Name the blood parasite species.
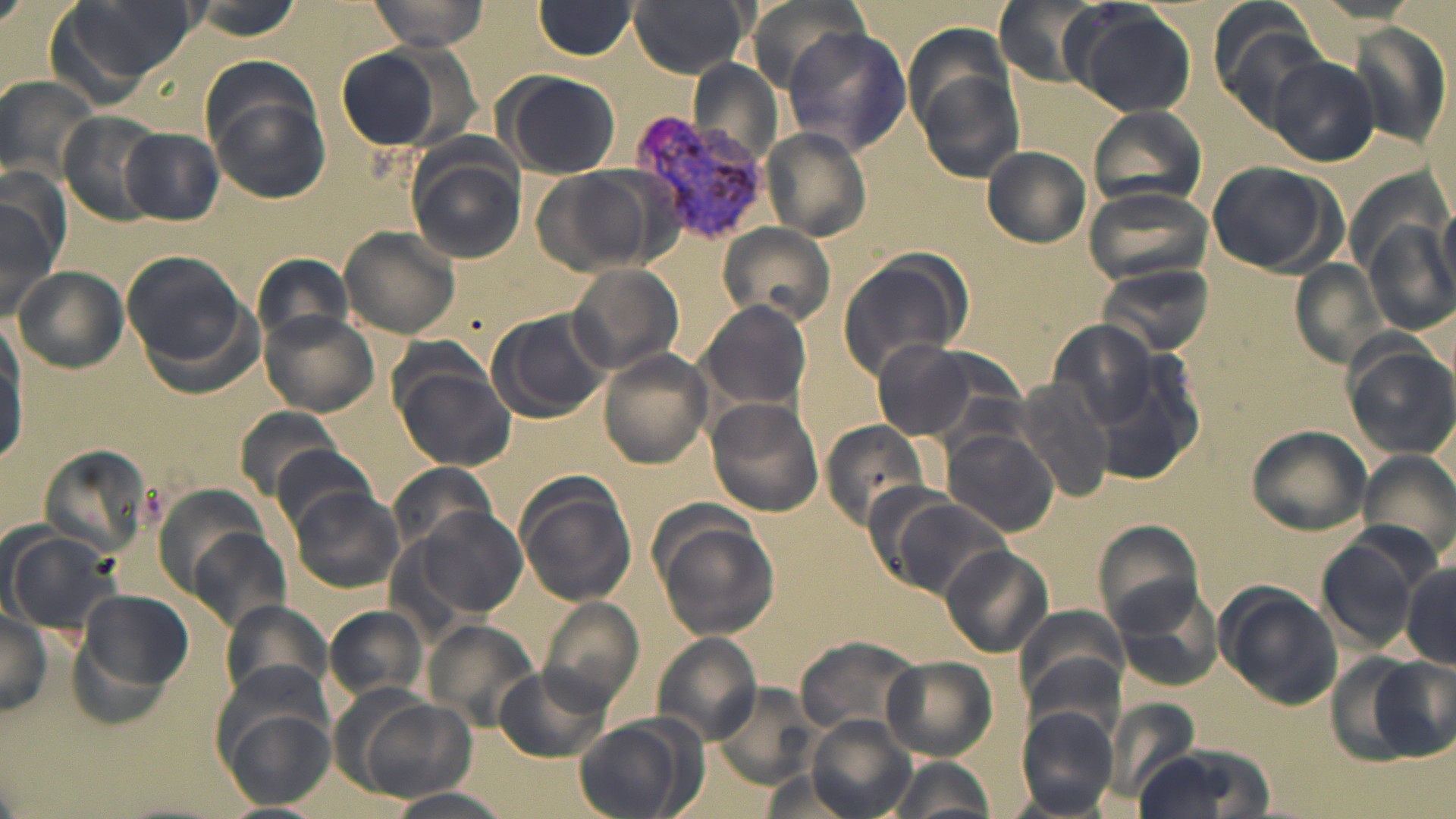
Plasmodium vivax.

preparation: thin blood smear
modality: light microscopy
image_size: 1456×819 pixels
uninfected_red_blood_cell_locations: 'approximate bounding boxes as named x1/y1/x2/y2 corners in pixels: (x1=49, y1=0, x2=195, y2=100), (x1=365, y1=0, x2=487, y2=51), (x1=628, y1=0, x2=749, y2=77), (x1=992, y1=0, x2=1108, y2=86), (x1=535, y1=1, x2=638, y2=60), (x1=1067, y1=5, x2=1198, y2=118), (x1=1210, y1=7, x2=1334, y2=126), (x1=1350, y1=18, x2=1455, y2=154), (x1=780, y1=26, x2=911, y2=156), (x1=336, y1=46, x2=450, y2=151), (x1=1266, y1=56, x2=1377, y2=165), (x1=689, y1=57, x2=781, y2=168), (x1=912, y1=62, x2=1027, y2=186), (x1=499, y1=70, x2=622, y2=179), (x1=0, y1=74, x2=98, y2=184), (x1=202, y1=75, x2=331, y2=203), (x1=1086, y1=106, x2=1209, y2=213), (x1=59, y1=110, x2=166, y2=226), (x1=762, y1=127, x2=873, y2=241), (x1=122, y1=128, x2=223, y2=224), (x1=981, y1=146, x2=1091, y2=249), (x1=405, y1=153, x2=525, y2=263), (x1=1205, y1=160, x2=1344, y2=276), (x1=1, y1=165, x2=70, y2=276), (x1=534, y1=168, x2=662, y2=275), (x1=1082, y1=184, x2=1214, y2=290), (x1=0, y1=197, x2=61, y2=322), (x1=1438, y1=197, x2=1455, y2=300), (x1=1364, y1=216, x2=1455, y2=334), (x1=717, y1=225, x2=836, y2=326), (x1=338, y1=226, x2=462, y2=339), (x1=122, y1=250, x2=253, y2=374), (x1=836, y1=254, x2=971, y2=379), (x1=249, y1=257, x2=357, y2=347), (x1=1286, y1=259, x2=1394, y2=372), (x1=568, y1=263, x2=684, y2=374), (x1=1098, y1=263, x2=1217, y2=358), (x1=12, y1=266, x2=128, y2=373), (x1=700, y1=300, x2=812, y2=413), (x1=487, y1=307, x2=613, y2=422), (x1=258, y1=311, x2=378, y2=418), (x1=1039, y1=315, x2=1196, y2=461), (x1=0, y1=328, x2=26, y2=461), (x1=868, y1=337, x2=1009, y2=442), (x1=1344, y1=342, x2=1455, y2=458), (x1=598, y1=350, x2=713, y2=467), (x1=392, y1=362, x2=515, y2=472), (x1=1014, y1=380, x2=1119, y2=503), (x1=704, y1=398, x2=824, y2=517), (x1=234, y1=406, x2=348, y2=500), (x1=820, y1=417, x2=933, y2=532), (x1=1245, y1=423, x2=1374, y2=537), (x1=943, y1=430, x2=1059, y2=537), (x1=270, y1=440, x2=383, y2=535), (x1=42, y1=441, x2=159, y2=551), (x1=1361, y1=450, x2=1452, y2=564), (x1=388, y1=462, x2=499, y2=556), (x1=514, y1=478, x2=637, y2=607), (x1=287, y1=484, x2=404, y2=594), (x1=883, y1=495, x2=1014, y2=599), (x1=419, y1=507, x2=528, y2=616), (x1=654, y1=518, x2=776, y2=641), (x1=1089, y1=521, x2=1204, y2=637), (x1=186, y1=524, x2=291, y2=638), (x1=6, y1=527, x2=118, y2=636), (x1=1316, y1=533, x2=1427, y2=653), (x1=939, y1=546, x2=1052, y2=658), (x1=1399, y1=560, x2=1456, y2=669), (x1=1115, y1=583, x2=1227, y2=693), (x1=1218, y1=585, x2=1345, y2=708), (x1=78, y1=589, x2=194, y2=699), (x1=540, y1=594, x2=645, y2=709), (x1=219, y1=599, x2=330, y2=702), (x1=0, y1=603, x2=51, y2=719), (x1=327, y1=605, x2=427, y2=702), (x1=1020, y1=613, x2=1124, y2=738), (x1=424, y1=620, x2=538, y2=731), (x1=650, y1=632, x2=762, y2=743), (x1=796, y1=633, x2=919, y2=741), (x1=1366, y1=655, x2=1453, y2=763), (x1=884, y1=657, x2=996, y2=759), (x1=495, y1=665, x2=610, y2=764), (x1=714, y1=685, x2=817, y2=788), (x1=1111, y1=695, x2=1201, y2=801), (x1=349, y1=696, x2=477, y2=803), (x1=219, y1=706, x2=336, y2=809), (x1=1017, y1=706, x2=1120, y2=815), (x1=572, y1=716, x2=697, y2=818), (x1=805, y1=716, x2=916, y2=819), (x1=1133, y1=742, x2=1276, y2=819), (x1=883, y1=754, x2=996, y2=819), (x1=755, y1=766, x2=870, y2=817), (x1=380, y1=788, x2=516, y2=819), (x1=213, y1=803, x2=325, y2=819)'
magnification: 1000x
stain: May-Grünwald-Giemsa
field_of_view: single
plasmodium_vivax_infected_red_blood_cell_locations: 'approximate bounding boxes as named x1/y1/x2/y2 corners in pixels: (x1=632, y1=111, x2=778, y2=254)'